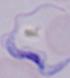

{
  "modality": "micrograph",
  "magnification": "1000x",
  "identification": "trypanosome"
}